State which parasite is depicted.
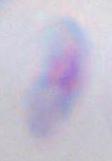
Toxoplasma gondii.

modality: photomicrograph
magnification: 1000x